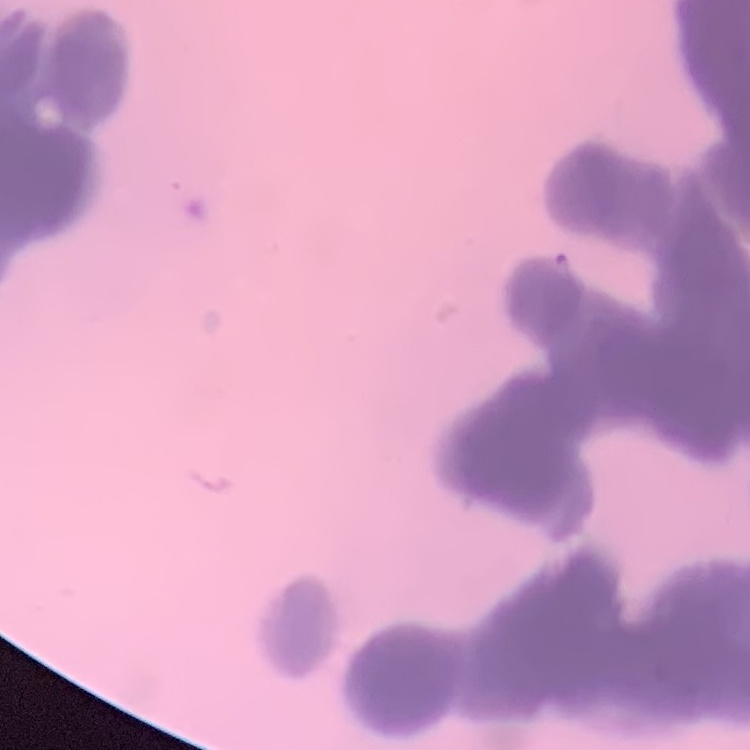

The red blood cells show rouleaux formation. Square crop of a larger photomicrograph. Field's or Giemsa stain. Thin blood film.